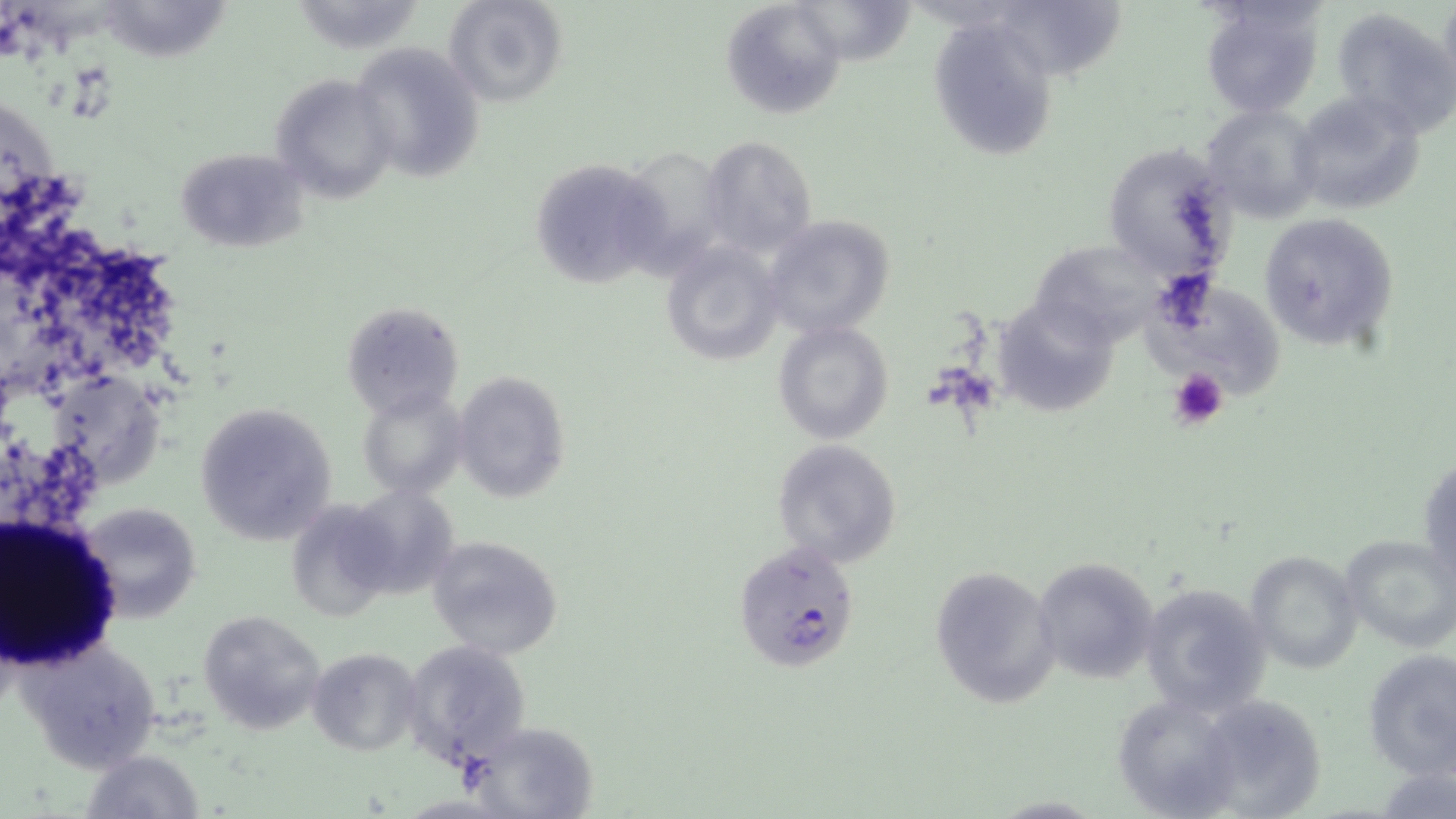

Summary:
  - Coordinate format: approximate bounding boxes as [x1, y1, x2, y2] in pixels
  - Plasmodium falciparum-infected red blood cell locations: [733, 542, 861, 673]
  - Platelet locations: [1168, 366, 1229, 429]
  - Uninfected red blood cell locations: [302, 0, 428, 56], [444, 0, 569, 109], [798, 0, 920, 67], [1007, 0, 1136, 84], [106, 1, 245, 66], [721, 1, 845, 118], [1198, 1, 1324, 118], [1331, 9, 1455, 136], [927, 18, 1058, 161], [350, 40, 486, 186], [270, 72, 396, 205], [1288, 91, 1425, 215], [1200, 104, 1323, 221], [697, 135, 818, 259], [1102, 142, 1239, 284], [615, 146, 735, 273], [174, 147, 308, 252], [529, 156, 672, 289], [1258, 211, 1398, 348], [760, 214, 894, 338], [659, 239, 784, 367], [1028, 241, 1168, 346], [1145, 277, 1298, 403], [340, 300, 465, 421], [997, 305, 1129, 418], [772, 320, 893, 445], [47, 370, 176, 491], [453, 371, 572, 504], [357, 390, 467, 498], [195, 400, 338, 544], [771, 438, 903, 568], [342, 486, 462, 600], [74, 502, 202, 622], [285, 502, 398, 620], [1340, 532, 1456, 654], [425, 533, 565, 661], [1245, 550, 1363, 675], [1032, 557, 1160, 685], [928, 565, 1058, 709], [1138, 580, 1273, 716], [198, 610, 326, 735], [16, 633, 164, 774], [400, 639, 533, 769], [307, 648, 421, 756], [1361, 650, 1456, 778], [1112, 692, 1244, 819], [1181, 693, 1329, 818], [473, 723, 595, 818], [81, 750, 205, 819]
  - Slide-level diagnosis: Plasmodium falciparum
  - Image size: 1456×819 pixels
  - Field of view: one of a larger specimen
  - Modality: optical microscopy
  - Preparation: thin blood film
  - Magnification: 1000x
  - Stain: May-Grünwald-Giemsa